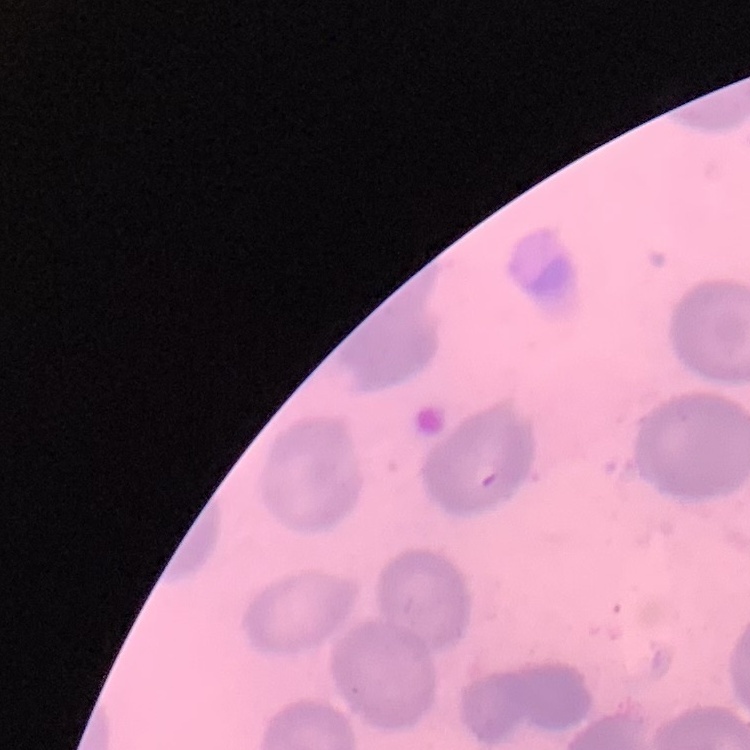

Summary:
  - Red blood cell morphology: no rouleaux formation
  - Preparation: thin blood smear
  - Image type: one tile cut from a larger photomicrograph
  - Stain: Field's or Giemsa